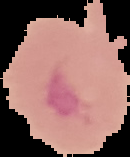

preparation = thin blood film
image type = segmented cell region on a black background
malaria status = uninfected
image size = 130×157 pixels